Assess the morphology of the erythrocytes.
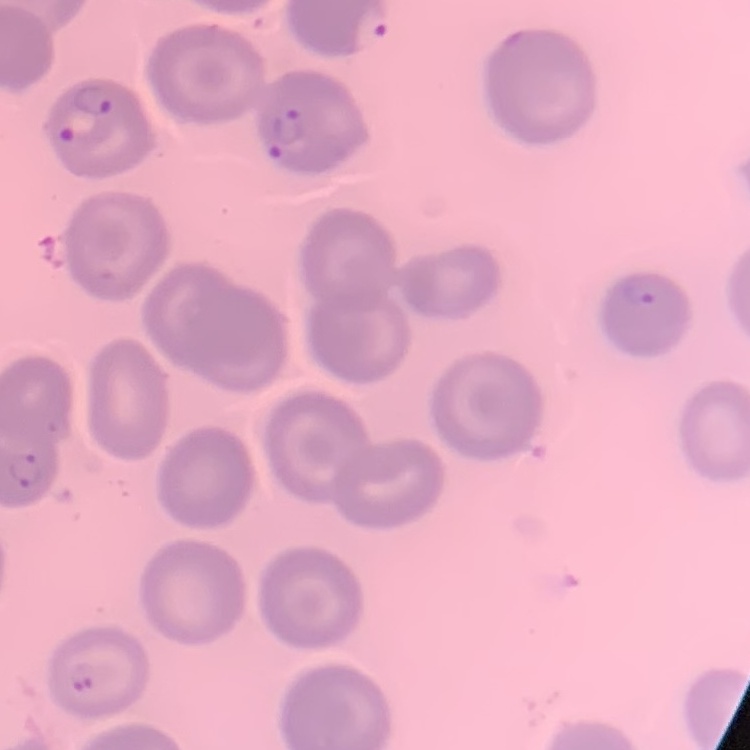

No rouleaux formation.

Summary:
  - Stain: Field's or Giemsa
  - Preparation: thin blood smear
  - Image type: square crop of a larger photomicrograph